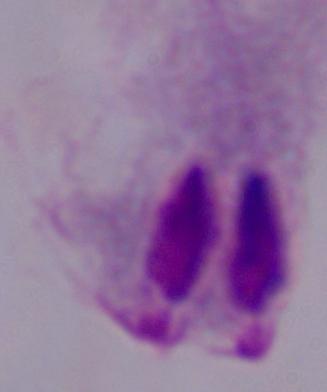 A trichomonad is seen. Captured at 1000x magnification. Photomicrograph.